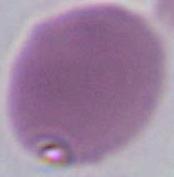

Summary:
  - Identification: erythrocyte
  - Modality: micrograph
  - Magnification: 1000x